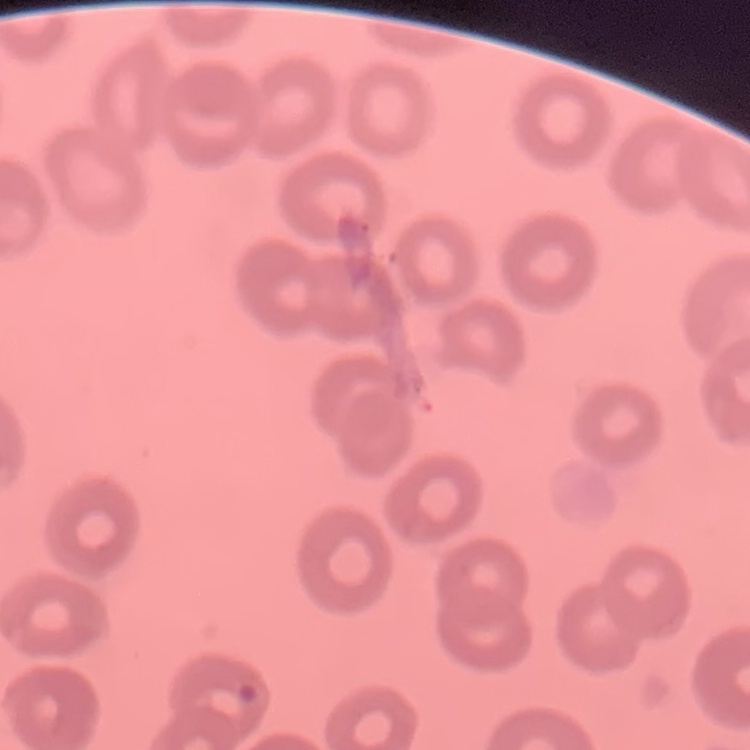
Summary:
  - Red blood cell morphology: no rouleaux formation
  - Preparation: thin peripheral smear
  - Stain: Field's or Giemsa
  - Image type: square crop of a larger photomicrograph